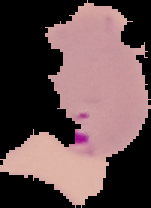 Image is 151×208 pixels. Segmented cell region on a black background. From a thin blood film. Result: Plasmodium parasites identified.